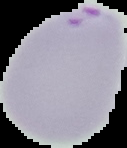
Summary:
  - Image type: segmented cell region with the area outside set to black
  - Malaria status: parasitized
  - Preparation: thin blood film
  - Image size: 127×148 pixels